Outline each blood parasite and name the species.
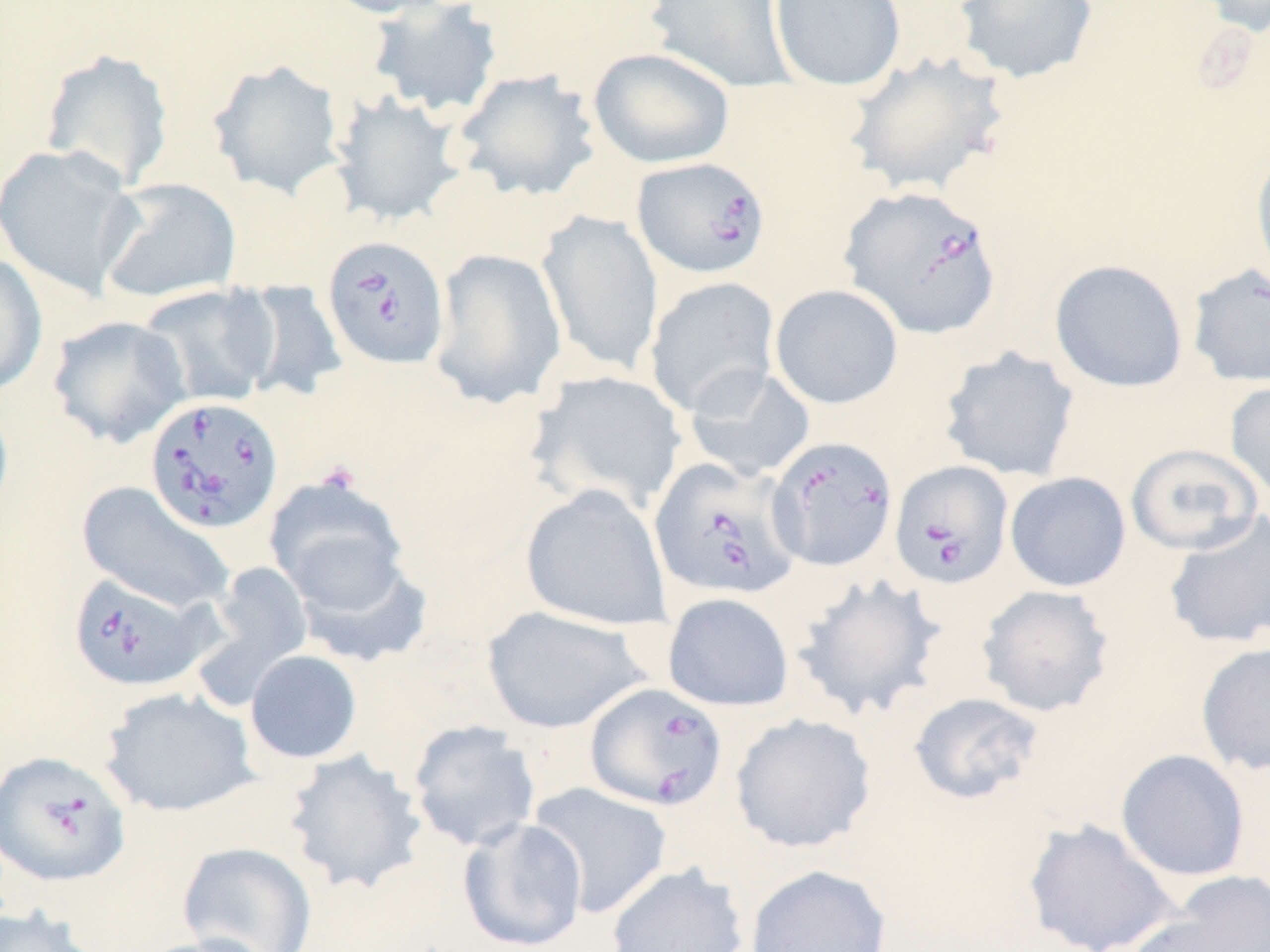

Approximate bounding boxes as (x1,y1)-(x2,y2) corner pairs in pixels.
Babesia divergens-infected red blood cells: (632,157)-(770,279), (839,185)-(1003,338), (322,235)-(450,370), (144,396)-(284,534), (766,435)-(898,572), (649,457)-(801,601), (889,460)-(1014,589), (66,572)-(210,692), (585,682)-(728,811), (0,750)-(132,888).
No Plasmodium falciparum, Plasmodium ovale, Plasmodium malariae, Plasmodium vivax, or Trypanosoma brucei observed.

{
  "slide_level_diagnosis": "Babesia divergens",
  "stain": "May-Grünwald-Giemsa",
  "field_of_view": "one of a larger specimen",
  "uninfected_red_blood_cell_locations": "approximate bounding boxes as (x1,y1)-(x2,y2) corner pairs in pixels: (316,0)-(462,19), (644,0)-(797,92), (768,0)-(906,91), (1195,0)-(1270,37), (364,1)-(503,119), (953,1)-(1100,84), (588,47)-(736,169), (39,48)-(175,191), (842,50)-(1013,199), (207,59)-(346,199), (452,68)-(601,203), (328,92)-(467,227), (0,143)-(143,300), (1250,143)-(1270,287), (97,177)-(242,304), (537,209)-(664,377), (429,247)-(567,410), (0,251)-(48,396), (1049,259)-(1189,393), (1186,263)-(1270,388), (644,276)-(780,416), (232,280)-(349,404), (137,283)-(281,409), (770,284)-(904,409), (47,315)-(191,448), (939,345)-(1080,482), (683,364)-(816,482), (527,370)-(688,515), (1225,379)-(1270,502), (0,394)-(14,521), (1126,443)-(1266,555), (1005,472)-(1131,592), (265,476)-(411,612), (76,481)-(235,615), (521,484)-(671,630), (1163,512)-(1270,650), (287,545)-(434,667), (195,561)-(314,704), (792,572)-(947,722), (976,584)-(1115,718), (662,592)-(795,711), (481,605)-(650,734), (1195,641)-(1270,776), (244,650)-(363,764), (99,687)-(260,817), (908,691)-(1045,805), (730,713)-(876,853), (407,720)-(540,852), (282,749)-(429,896), (1115,749)-(1250,882), (528,783)-(672,919), (457,817)-(588,951), (1022,818)-(1180,952), (177,841)-(318,952), (606,862)-(748,952), (745,863)-(892,952), (1140,870)-(1270,951), (0,906)-(99,952), (130,934)-(278,952)",
  "preparation": "thin blood smear",
  "modality": "optical microscopy",
  "image_size": "1270×952 pixels",
  "magnification": "1000x",
  "platelet_locations": "approximate bounding boxes as (x1,y1)-(x2,y2) corner pairs in pixels: (316,460)-(362,495)"
}